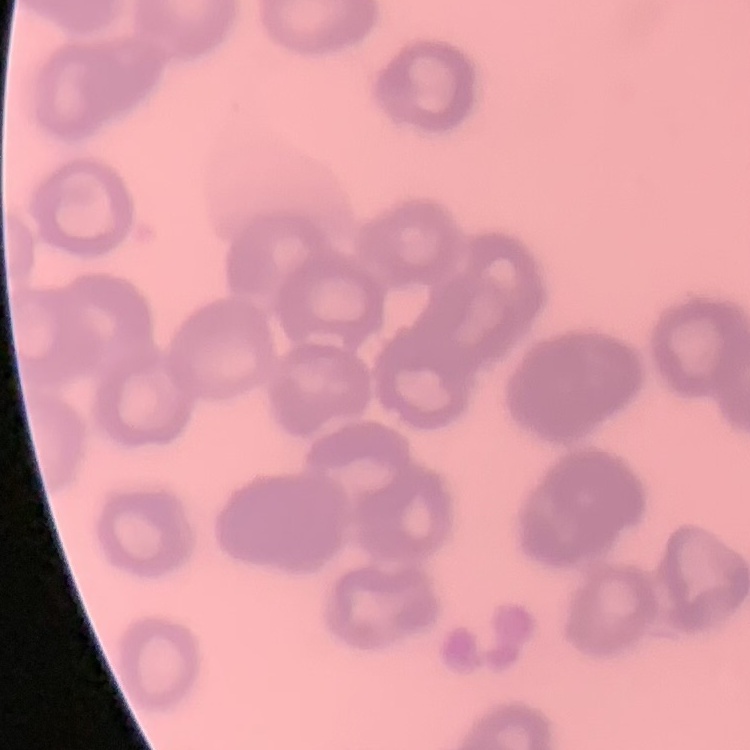

Summary:
  - Erythrocyte morphology: rouleaux formation
  - Image type: square crop of a larger photomicrograph
  - Stain: Field's or Giemsa
  - Preparation: thin blood smear